Assess this cell for malaria.
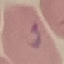

It is parasitized.

Giemsa stain. Automatically extracted cell patch, resized to 64 × 64 pixels. Acquired by smartphone through the microscope eyepiece. Thin blood film.